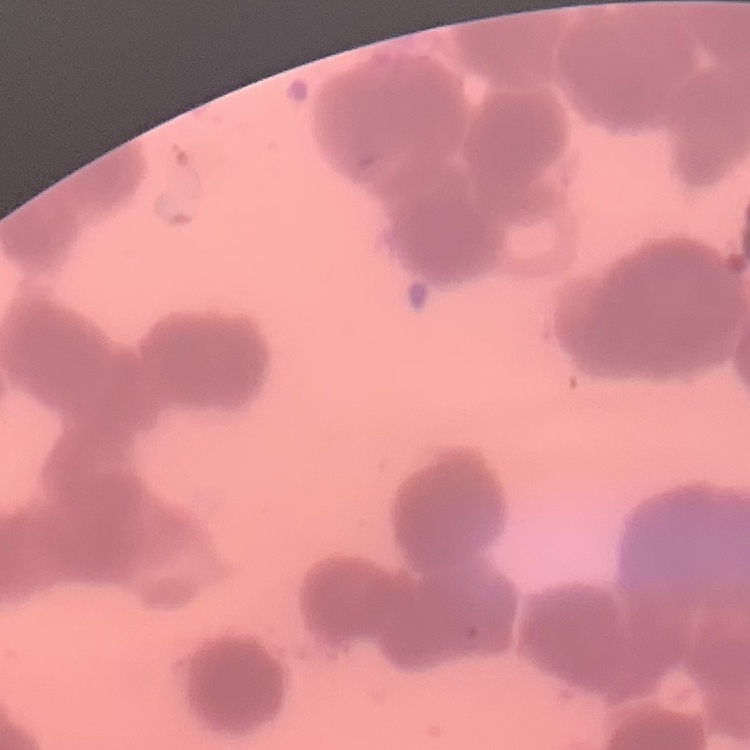

erythrocyte morphology = rouleaux formation
stain = Field's or Giemsa
preparation = thin peripheral smear
image type = square crop of a larger photomicrograph